Report the malaria status of this cell.
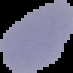
Uninfected.

Image is 73×73 pixels. From a thin blood smear. Segmented cell region on a black background.